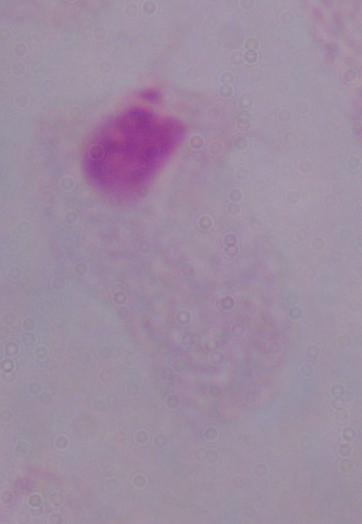

Summary:
  - Identification: trichomonad
  - Magnification: 1000x
  - Modality: photomicrograph